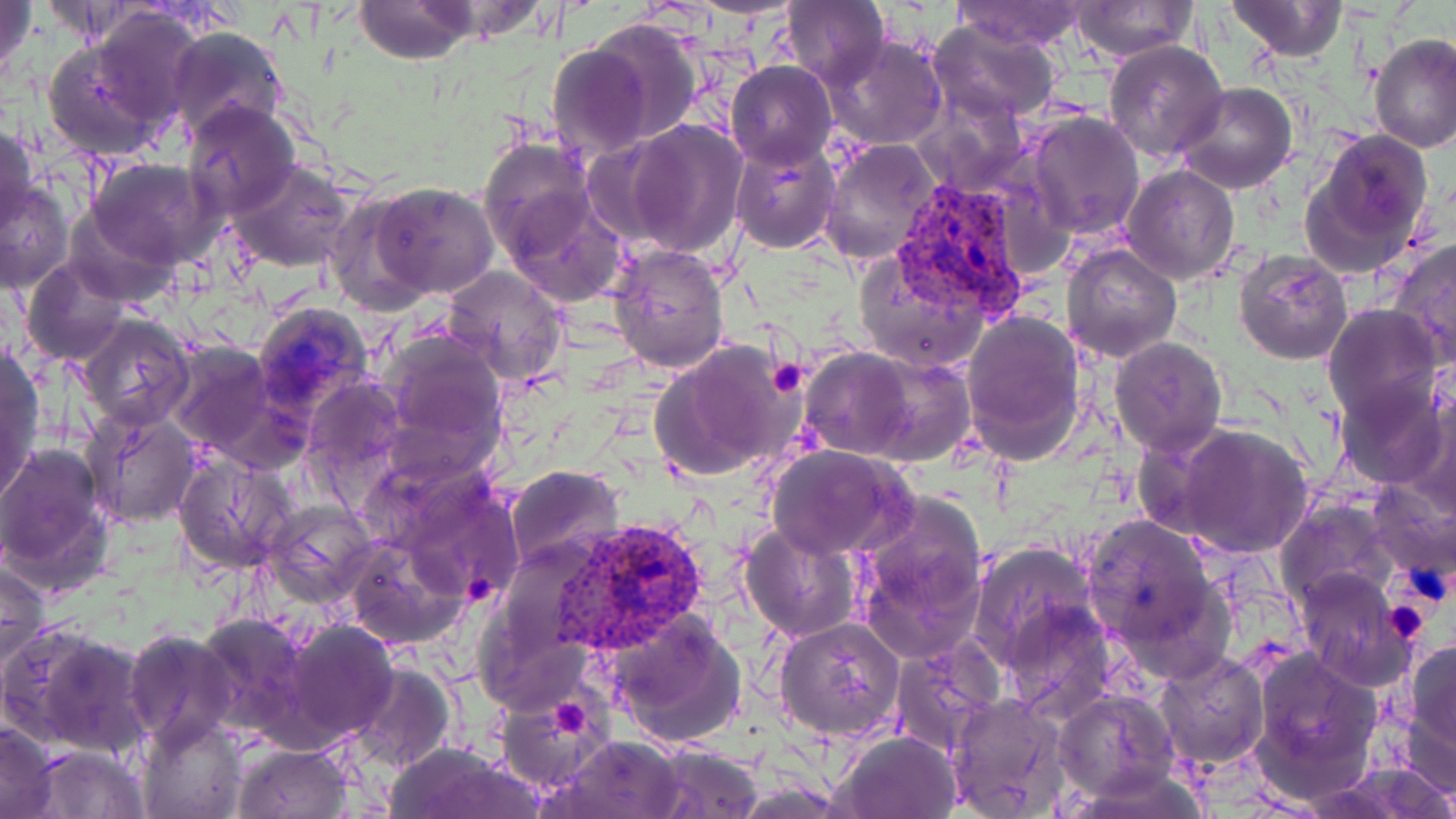

Approximate bounding boxes as [x1, y1, x2, y2] in pixels. Plasmodium vivax-infected red blood cell locations: [892, 174, 1034, 319], [553, 514, 710, 654]. Uninfected red blood cell locations: [1, 0, 37, 91], [354, 0, 480, 65], [945, 0, 1089, 50], [1226, 0, 1346, 61], [776, 1, 891, 87], [1069, 3, 1197, 61], [92, 6, 209, 128], [928, 19, 1058, 122], [583, 20, 704, 145], [165, 27, 290, 146], [1369, 33, 1455, 155], [43, 35, 173, 159], [822, 35, 948, 152], [1104, 39, 1228, 162], [546, 41, 656, 160], [725, 60, 837, 168], [1175, 83, 1298, 195], [915, 91, 1028, 196], [183, 101, 302, 219], [1026, 112, 1145, 240], [622, 120, 749, 257], [0, 123, 39, 241], [1300, 128, 1434, 274], [478, 138, 600, 267], [818, 138, 944, 268], [730, 140, 842, 254], [85, 158, 220, 269], [229, 161, 353, 273], [1120, 164, 1241, 284], [0, 180, 74, 295], [370, 181, 499, 299], [499, 187, 623, 310], [326, 194, 435, 312], [62, 210, 181, 304], [1388, 238, 1455, 366], [607, 242, 731, 374], [1061, 243, 1183, 364], [853, 248, 992, 374], [1234, 249, 1355, 365], [20, 257, 132, 365], [441, 264, 569, 389], [253, 300, 376, 417], [1323, 304, 1442, 421], [961, 309, 1087, 465], [75, 314, 196, 430], [379, 327, 509, 462], [1110, 336, 1228, 457], [651, 339, 807, 483], [163, 340, 287, 462], [1, 343, 45, 498], [798, 349, 918, 459], [864, 357, 974, 466], [1336, 374, 1449, 488], [302, 376, 408, 497], [1405, 392, 1456, 518], [82, 409, 203, 528], [1172, 423, 1313, 559], [0, 442, 113, 592], [766, 444, 916, 560], [174, 452, 297, 574], [381, 458, 530, 606], [503, 465, 626, 574], [1364, 476, 1456, 584], [850, 494, 991, 663], [262, 498, 380, 608], [1277, 501, 1397, 612], [1081, 514, 1228, 670], [740, 521, 861, 642], [345, 532, 472, 648], [968, 540, 1103, 679], [0, 559, 49, 674], [1294, 568, 1410, 686], [997, 593, 1119, 722], [603, 608, 746, 750], [194, 610, 313, 739], [776, 616, 906, 742], [276, 619, 398, 745], [3, 623, 153, 757], [123, 629, 240, 750], [890, 635, 1005, 754], [1403, 636, 1456, 767], [1248, 647, 1383, 802], [1154, 651, 1270, 772], [347, 660, 457, 775], [498, 690, 619, 802], [1055, 690, 1177, 802], [945, 694, 1071, 818], [135, 715, 250, 819], [0, 720, 60, 819], [836, 731, 961, 819], [550, 734, 687, 819], [231, 743, 352, 819], [385, 743, 540, 819], [642, 743, 764, 819], [30, 744, 149, 818], [1314, 762, 1456, 819], [1062, 765, 1218, 818]. Platelet locations: [767, 360, 807, 399], [1382, 599, 1431, 642], [550, 696, 595, 740]. Slide-level diagnosis: Plasmodium vivax. Single field of view. Thin blood smear. Image is 1456×819 pixels. Optical microscopy. Captured at 1000x magnification. May-Grünwald-Giemsa-stained preparation.